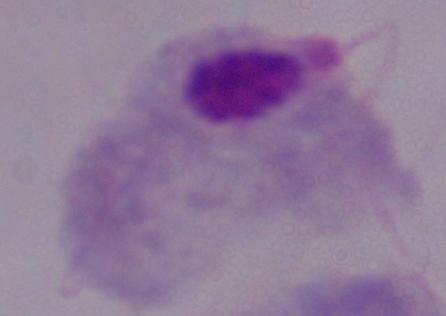

1000x magnification. A trichomonad is shown. Micrograph.